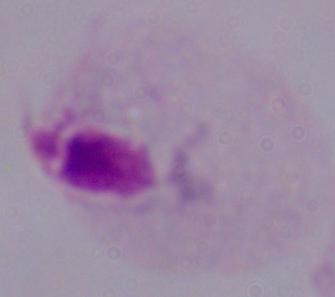

modality: micrograph
identification: trichomonad
magnification: 1000x